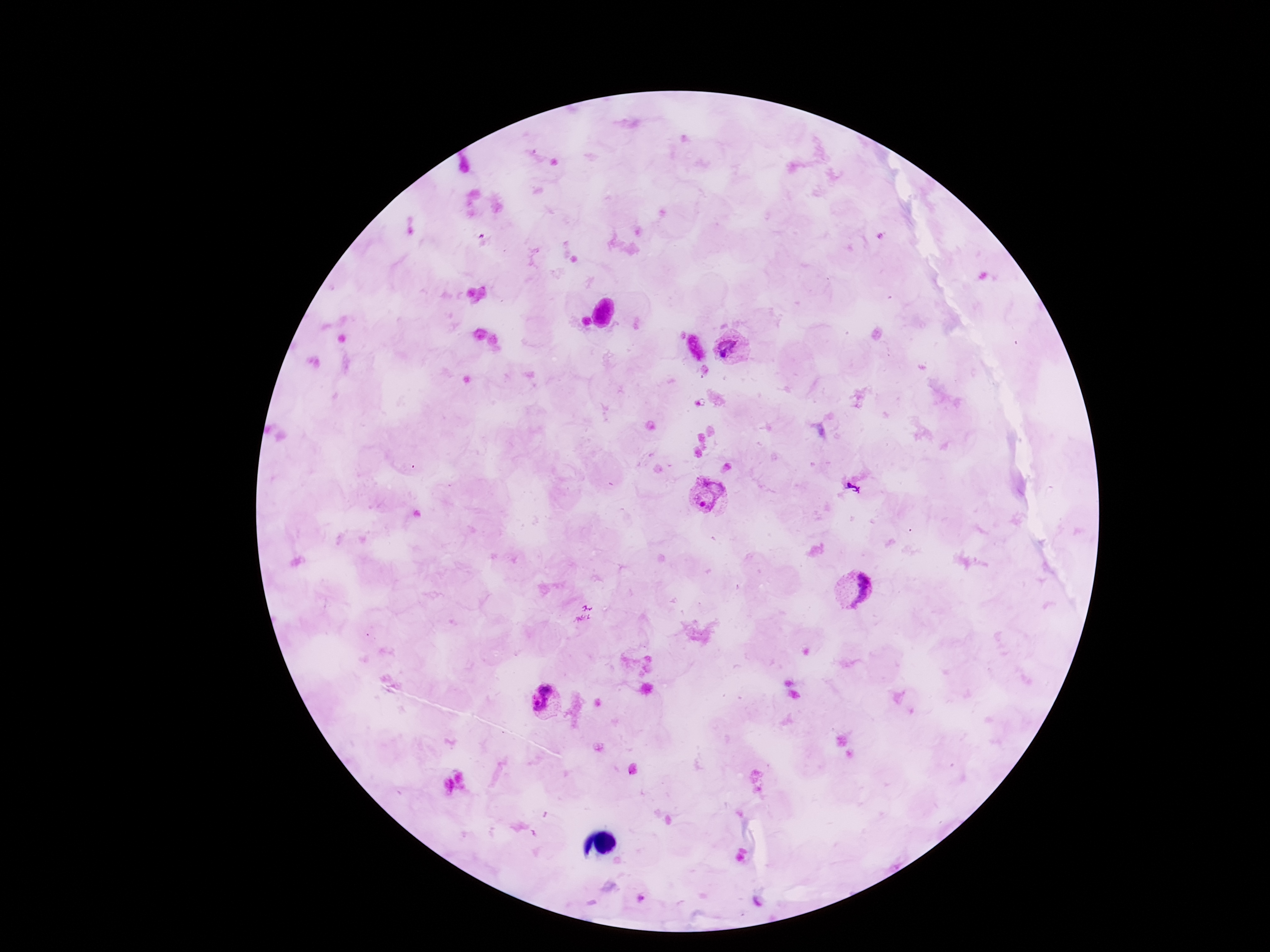
Approximate object centers, in pixels from the top-left corner.
Summary:
  - Plasmodium parasite locations: (x=733, y=348), (x=710, y=498), (x=855, y=591), (x=546, y=698)
  - Preparation: thick blood smear
  - Capture: smartphone camera through the microscope eyepiece
  - Stain: Giemsa
  - Field of view: single
  - Image size: 1270×952 pixels
  - Magnification: 100x
  - Patient malaria status: infected